Classify this cell by malaria status.
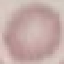
Uninfected.

{
  "stain": "Giemsa",
  "capture": "smartphone camera at the microscope eyepiece",
  "image_type": "automatically extracted cell patch, resized to 64 × 64 pixels",
  "preparation": "thin blood smear"
}